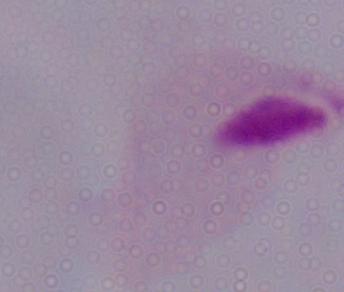
Summary:
  - Magnification: 1000x
  - Modality: micrograph
  - Identification: trichomonad